Give the extent of all uninfected red blood cells.
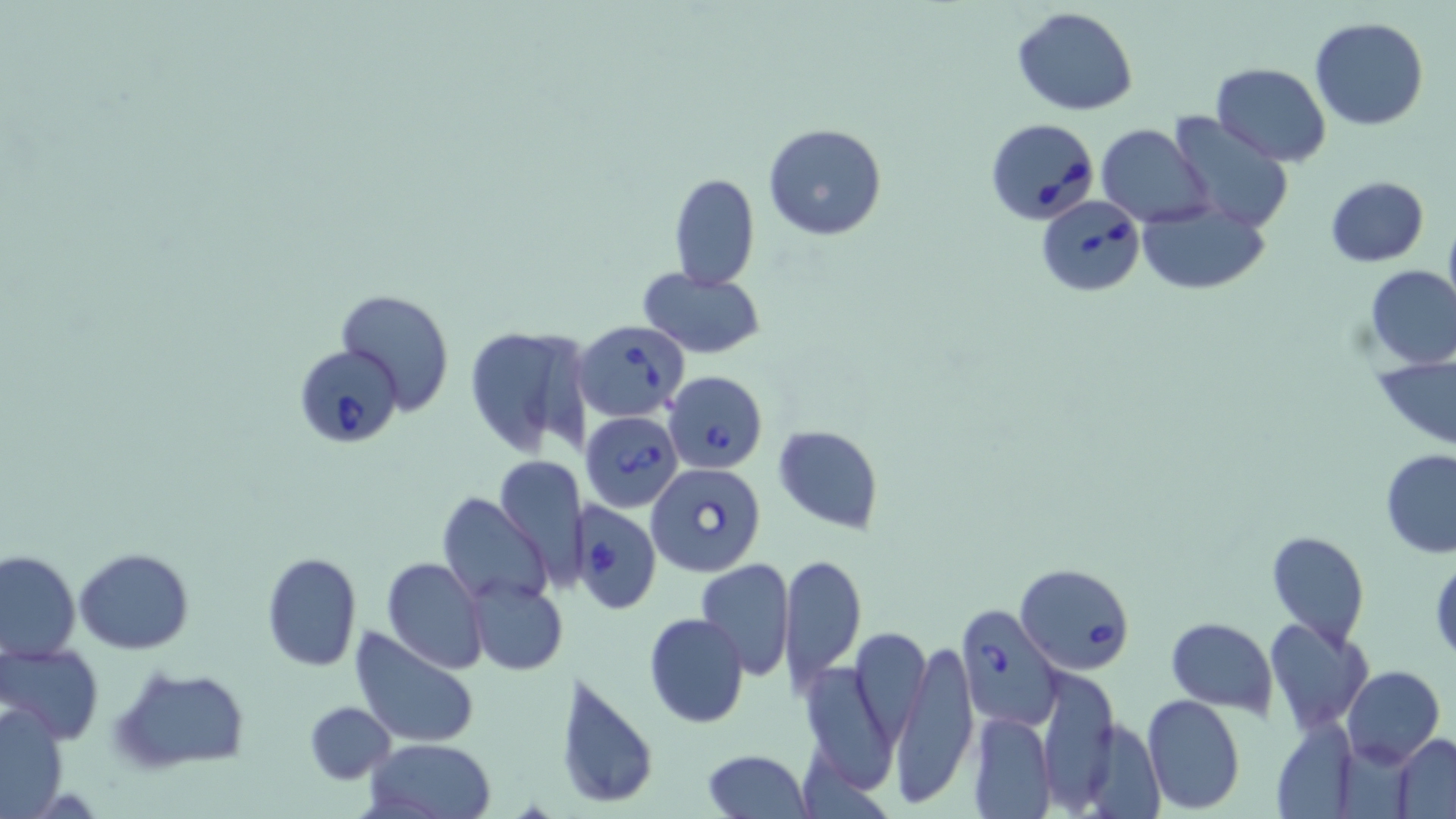

Approximate bounding boxes as (x1, y1, x2, y2) in pixels.
Uninfected red blood cells: (1012, 6, 1138, 115), (1309, 17, 1430, 131), (1209, 62, 1332, 165), (1165, 113, 1294, 233), (762, 123, 888, 241), (1096, 125, 1215, 227), (669, 174, 760, 289), (1324, 176, 1429, 267), (1136, 199, 1270, 296), (1443, 213, 1456, 318), (1364, 265, 1456, 367), (639, 269, 766, 358), (333, 288, 456, 413), (462, 322, 596, 458), (1374, 355, 1456, 447), (774, 425, 882, 531), (1380, 449, 1456, 558), (496, 454, 587, 582), (439, 492, 553, 609), (1268, 530, 1369, 647), (74, 547, 194, 653), (0, 550, 80, 660), (260, 552, 362, 672), (778, 553, 867, 690), (1430, 555, 1455, 660), (381, 557, 488, 673), (694, 559, 795, 680), (466, 579, 567, 674), (644, 612, 749, 728), (1265, 616, 1372, 734), (1167, 617, 1277, 714), (351, 627, 480, 749), (852, 627, 931, 745), (890, 638, 979, 805), (0, 642, 103, 745), (798, 659, 898, 794), (111, 665, 250, 775), (1342, 666, 1444, 768), (556, 669, 659, 813), (1036, 674, 1115, 819), (1142, 694, 1245, 811), (2, 700, 70, 816), (305, 701, 395, 783), (969, 711, 1057, 817), (1271, 718, 1360, 817), (1078, 720, 1162, 816), (1392, 733, 1456, 816), (363, 738, 499, 819), (703, 748, 812, 818).

slide_level_diagnosis: Babesia divergens
magnification: 1000x
image_size: 1456×819 pixels
babesia_divergens_infected_red_blood_cell_locations: 'approximate bounding boxes as (x1, y1, x2, y2) in pixels: (984, 116, 1101, 226), (1036, 197, 1144, 297), (575, 320, 689, 421), (293, 346, 404, 447), (664, 371, 767, 474), (580, 412, 683, 510), (647, 462, 765, 576), (575, 502, 659, 614), (1015, 564, 1137, 677), (956, 603, 1064, 729)'
modality: optical microscopy
field_of_view: single
stain: May-Grünwald-Giemsa
preparation: thin blood film